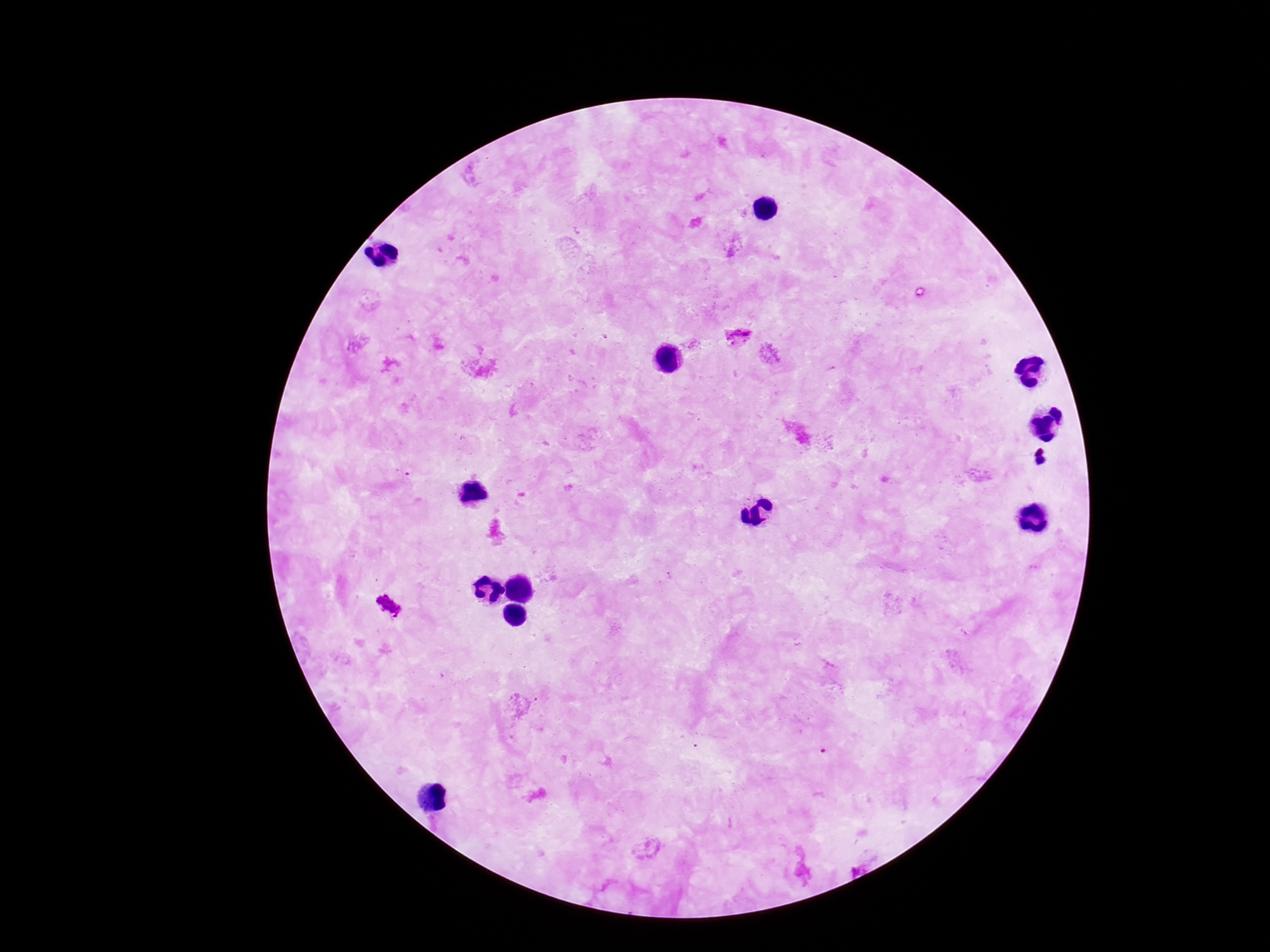
Approximate centers as [x, y] in pixels.
Summary:
  - Plasmodium parasite locations: [737, 337], [389, 605]
  - Field of view: single
  - Image size: 1270×952 pixels
  - Stain: Giemsa
  - Magnification: 100x
  - Capture: smartphone camera through the microscope eyepiece
  - Preparation: thick peripheral-blood smear
  - Patient malaria status: infected